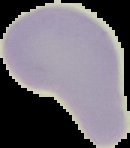

Malaria status: uninfected. Image is 130×148 pixels. From a thin blood film. Segmented cell region on a black background.